Locate and identify every blood parasite.
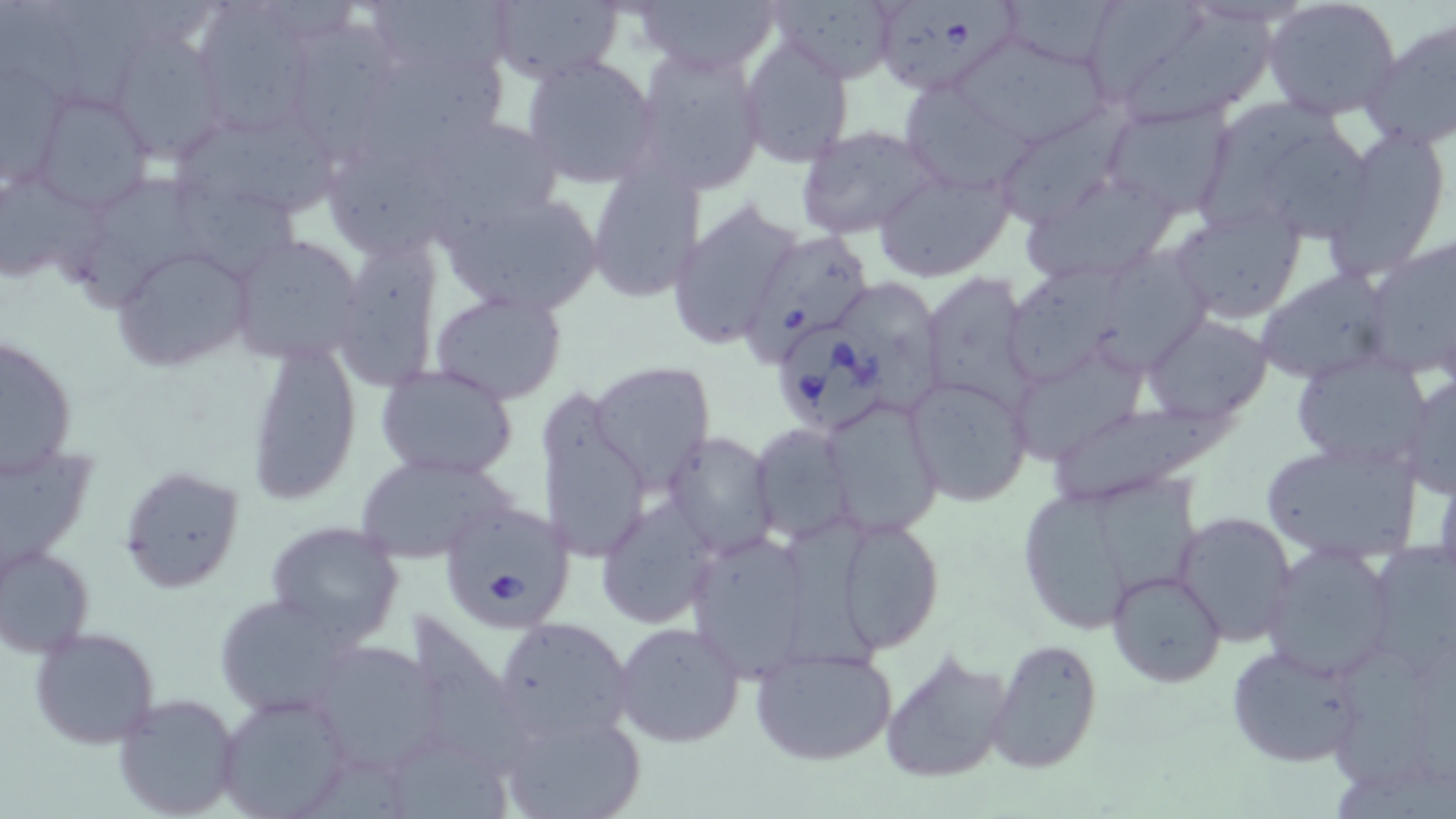
Approximate bounding boxes as named x1/y1/x2/y2 corners in pixels.
Babesia divergens-infected red blood cells: (x1=870, y1=0, x2=1019, y2=98), (x1=744, y1=231, x2=872, y2=368), (x1=773, y1=332, x2=890, y2=431), (x1=436, y1=500, x2=576, y2=631).
No Plasmodium falciparum, Plasmodium ovale, Plasmodium malariae, Plasmodium vivax, or Trypanosoma brucei observed.

Summary:
  - Uninfected red blood cell locations: (x1=47, y1=0, x2=143, y2=114), (x1=362, y1=0, x2=518, y2=88), (x1=634, y1=0, x2=782, y2=75), (x1=767, y1=0, x2=904, y2=80), (x1=995, y1=0, x2=1125, y2=71), (x1=1263, y1=0, x2=1403, y2=121), (x1=485, y1=1, x2=624, y2=82), (x1=0, y1=2, x2=80, y2=105), (x1=191, y1=3, x2=321, y2=138), (x1=1100, y1=4, x2=1281, y2=124), (x1=1363, y1=17, x2=1456, y2=152), (x1=300, y1=21, x2=400, y2=153), (x1=110, y1=28, x2=232, y2=162), (x1=738, y1=35, x2=856, y2=168), (x1=961, y1=35, x2=1109, y2=145), (x1=352, y1=41, x2=509, y2=164), (x1=629, y1=46, x2=769, y2=194), (x1=520, y1=55, x2=663, y2=189), (x1=0, y1=68, x2=68, y2=187), (x1=900, y1=80, x2=1036, y2=196), (x1=29, y1=89, x2=155, y2=213), (x1=1203, y1=98, x2=1339, y2=225), (x1=1101, y1=101, x2=1235, y2=219), (x1=989, y1=110, x2=1126, y2=229), (x1=173, y1=117, x2=339, y2=213), (x1=794, y1=126, x2=938, y2=240), (x1=1325, y1=129, x2=1454, y2=276), (x1=1287, y1=138, x2=1374, y2=245), (x1=586, y1=164, x2=704, y2=303), (x1=874, y1=166, x2=1014, y2=281), (x1=1021, y1=170, x2=1185, y2=286), (x1=0, y1=172, x2=97, y2=286), (x1=82, y1=176, x2=212, y2=310), (x1=180, y1=184, x2=298, y2=272), (x1=437, y1=190, x2=603, y2=315), (x1=669, y1=200, x2=803, y2=352), (x1=1169, y1=202, x2=1306, y2=323), (x1=228, y1=234, x2=367, y2=365), (x1=333, y1=234, x2=443, y2=388), (x1=1364, y1=236, x2=1455, y2=382), (x1=111, y1=244, x2=255, y2=370), (x1=1098, y1=250, x2=1213, y2=378), (x1=1014, y1=261, x2=1133, y2=381), (x1=1256, y1=270, x2=1397, y2=385), (x1=923, y1=273, x2=1034, y2=412), (x1=431, y1=289, x2=568, y2=404), (x1=1142, y1=315, x2=1273, y2=422), (x1=2, y1=333, x2=77, y2=479), (x1=246, y1=343, x2=362, y2=505), (x1=1009, y1=345, x2=1146, y2=464), (x1=1288, y1=355, x2=1434, y2=472), (x1=587, y1=361, x2=715, y2=491), (x1=376, y1=364, x2=517, y2=481), (x1=1399, y1=372, x2=1456, y2=498), (x1=907, y1=374, x2=1033, y2=507), (x1=538, y1=388, x2=650, y2=564), (x1=822, y1=396, x2=945, y2=535), (x1=1051, y1=402, x2=1227, y2=506), (x1=750, y1=424, x2=857, y2=543), (x1=662, y1=431, x2=778, y2=557), (x1=1259, y1=437, x2=1426, y2=566), (x1=0, y1=443, x2=98, y2=576), (x1=353, y1=455, x2=511, y2=565), (x1=118, y1=464, x2=245, y2=593), (x1=1103, y1=474, x2=1200, y2=593), (x1=1027, y1=490, x2=1130, y2=628), (x1=596, y1=500, x2=717, y2=628), (x1=1172, y1=511, x2=1298, y2=647), (x1=835, y1=514, x2=947, y2=653), (x1=265, y1=519, x2=406, y2=644), (x1=785, y1=520, x2=883, y2=673), (x1=684, y1=527, x2=817, y2=676), (x1=1367, y1=542, x2=1456, y2=676), (x1=0, y1=543, x2=95, y2=658), (x1=1261, y1=543, x2=1397, y2=680), (x1=1107, y1=569, x2=1226, y2=687), (x1=213, y1=593, x2=360, y2=716), (x1=408, y1=606, x2=525, y2=772), (x1=492, y1=615, x2=635, y2=745), (x1=610, y1=621, x2=747, y2=750), (x1=29, y1=626, x2=162, y2=750), (x1=306, y1=639, x2=446, y2=775), (x1=988, y1=639, x2=1103, y2=772), (x1=1334, y1=641, x2=1429, y2=790), (x1=1227, y1=644, x2=1366, y2=766), (x1=750, y1=646, x2=898, y2=765), (x1=877, y1=646, x2=1015, y2=786), (x1=214, y1=691, x2=353, y2=819), (x1=111, y1=692, x2=242, y2=819), (x1=497, y1=707, x2=647, y2=819), (x1=395, y1=749, x2=522, y2=817)
  - Slide-level diagnosis: Babesia divergens
  - Image size: 1456×819 pixels
  - Stain: May-Grünwald-Giemsa
  - Preparation: thin blood film
  - Modality: optical microscopy
  - Magnification: 1000x
  - Field of view: one of a larger specimen